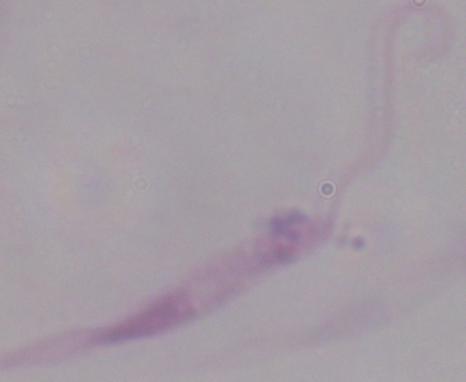
modality = photomicrograph
magnification = 1000x
identification = Leishmania